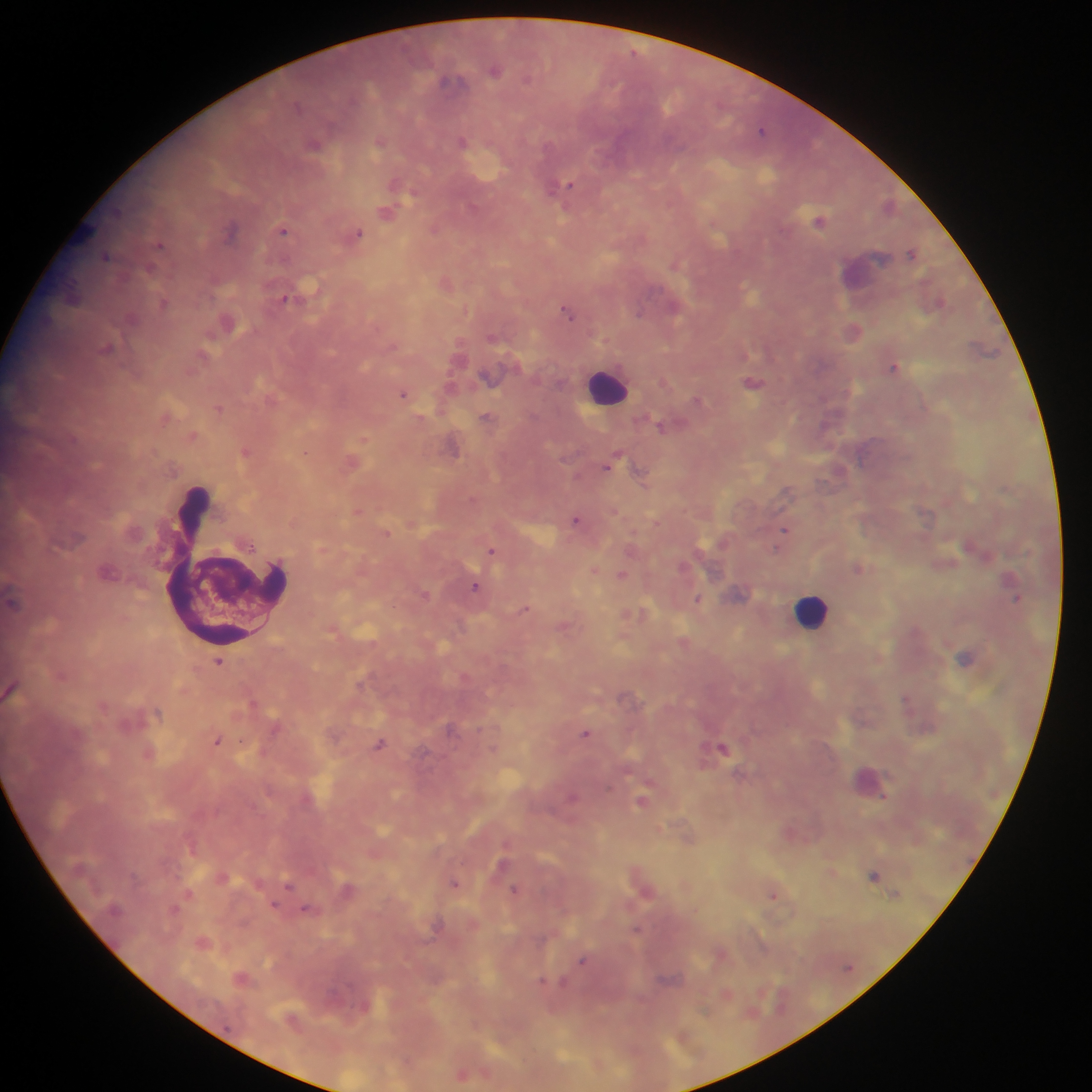

Approximate centers as (x, y) in pixels. Leukocyte locations: (607, 386), (812, 609). Malaria parasite locations: (634, 52), (494, 70), (527, 78), (447, 81), (298, 105), (762, 130), (462, 141), (379, 142), (314, 145), (394, 183), (564, 186), (554, 188), (387, 213), (819, 220), (435, 228), (231, 229), (284, 230), (358, 233), (160, 245), (912, 253), (105, 256), (674, 265), (149, 269), (285, 298), (163, 304), (639, 312), (568, 314), (107, 347), (894, 367), (753, 383), (403, 394), (697, 400), (485, 416), (660, 426), (825, 426), (453, 448), (245, 451), (305, 452), (610, 463), (576, 520), (783, 530), (388, 533), (778, 548), (491, 550), (859, 568), (594, 570), (622, 575), (475, 587), (425, 594), (1016, 598), (698, 599), (524, 609), (966, 657), (218, 662), (906, 698), (450, 728), (586, 733), (218, 740), (380, 744), (722, 748), (572, 798), (641, 801), (873, 876), (454, 883), (289, 884), (514, 890), (772, 895), (274, 905), (175, 908), (306, 909), (582, 960), (542, 981), (462, 1074). Mobile-phone photograph taken through the microscope. Collected in Ghana. Thick blood film. One field of view. Image is 1092×1092 pixels.